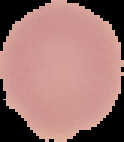

image_type: segmented cell region with the area outside set to black
result: no malaria parasites detected
preparation: thin blood film
image_size: 124×142 pixels